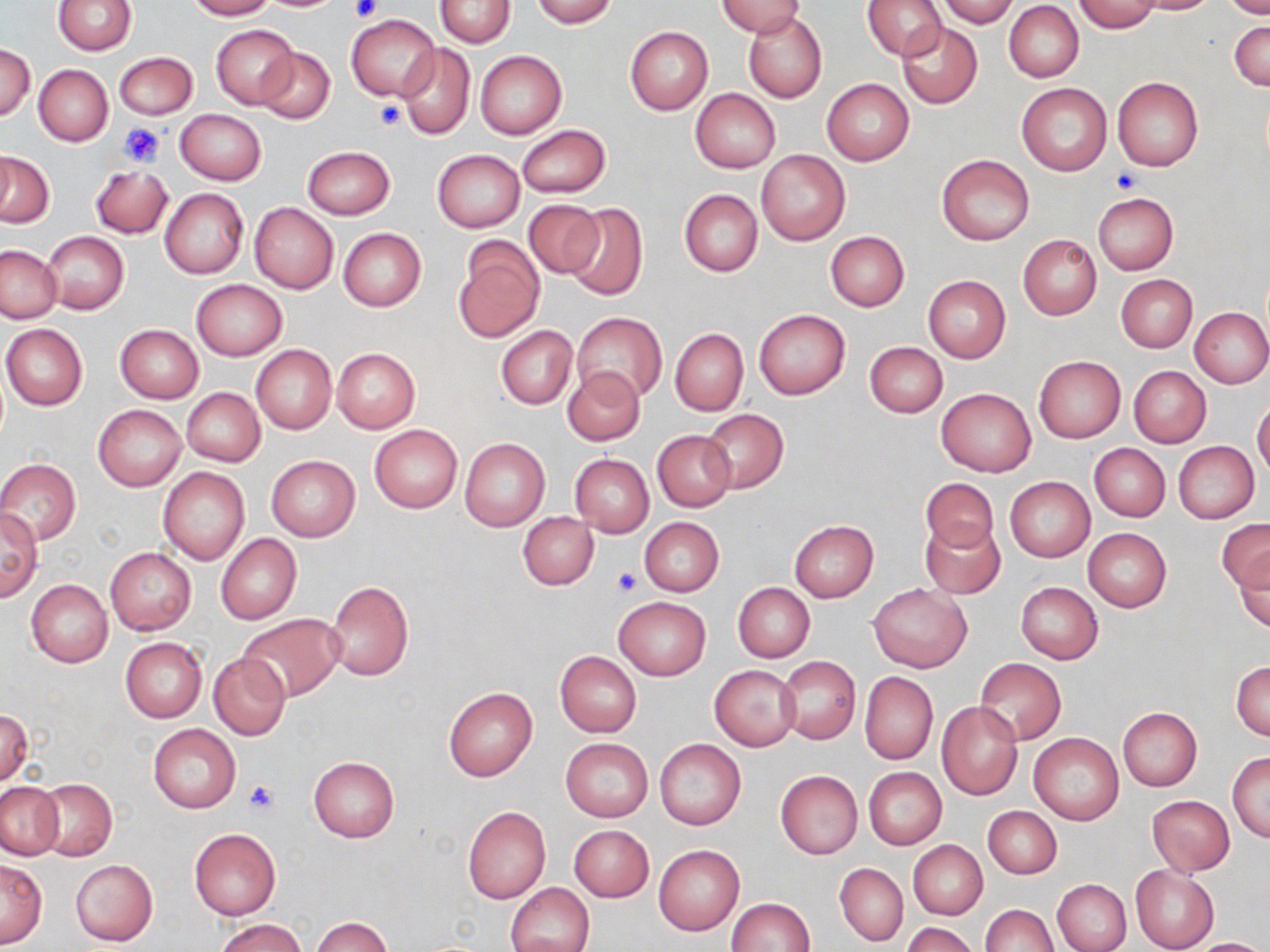
Approximate bounding boxes as [x1, y1, x2, y2] in pixels. Uninfected red blood cell locations: [53, 0, 135, 55], [184, 0, 275, 20], [435, 0, 515, 47], [531, 0, 619, 27], [715, 0, 807, 39], [863, 0, 948, 60], [937, 0, 1019, 27], [1128, 0, 1221, 14], [1219, 0, 1270, 19], [1071, 1, 1163, 33], [1004, 2, 1084, 82], [742, 11, 827, 104], [346, 14, 439, 102], [1229, 20, 1269, 90], [897, 22, 983, 108], [211, 24, 300, 109], [625, 25, 713, 115], [396, 42, 475, 139], [0, 44, 35, 121], [255, 47, 335, 123], [475, 51, 567, 138], [113, 52, 198, 120], [33, 64, 113, 145], [821, 78, 914, 165], [1112, 78, 1204, 171], [1017, 82, 1112, 175], [690, 88, 780, 174], [175, 109, 266, 185], [516, 124, 612, 198], [302, 146, 395, 219], [2, 147, 18, 222], [755, 148, 850, 245], [433, 150, 524, 233], [0, 151, 54, 227], [937, 153, 1033, 247], [90, 165, 172, 238], [159, 188, 248, 279], [679, 188, 763, 277], [1093, 192, 1178, 274], [523, 199, 604, 279], [248, 203, 339, 293], [563, 203, 648, 302], [338, 228, 426, 311], [825, 230, 910, 312], [42, 231, 128, 314], [1018, 235, 1101, 320], [454, 238, 545, 340], [1, 245, 62, 323], [1116, 274, 1197, 352], [923, 275, 1011, 362], [190, 279, 287, 360], [1189, 306, 1270, 388], [753, 308, 851, 400], [572, 312, 666, 405], [1, 323, 88, 410], [116, 324, 203, 403], [497, 326, 576, 409], [670, 328, 748, 415], [865, 341, 948, 417], [251, 345, 337, 434], [332, 348, 421, 434], [1034, 356, 1125, 442], [1129, 365, 1210, 447], [563, 367, 644, 444], [181, 388, 265, 468], [936, 388, 1035, 477], [1252, 398, 1270, 477], [93, 405, 186, 490], [699, 408, 789, 493], [369, 424, 463, 514], [651, 430, 737, 513], [459, 437, 550, 532], [1173, 441, 1259, 523], [1088, 442, 1170, 521], [569, 454, 653, 537], [266, 455, 359, 541], [0, 459, 81, 544], [157, 466, 250, 565], [919, 476, 998, 557], [1006, 476, 1096, 562], [0, 508, 43, 600], [517, 512, 599, 590], [639, 517, 724, 597], [790, 519, 879, 602], [920, 519, 1005, 599], [1217, 520, 1270, 593], [1083, 528, 1172, 611], [215, 533, 301, 625], [105, 547, 195, 635], [1232, 548, 1270, 631], [26, 580, 112, 667], [326, 580, 414, 681], [1015, 582, 1103, 664], [733, 583, 814, 663], [868, 583, 972, 673], [613, 597, 711, 679], [237, 613, 345, 702], [120, 637, 207, 723], [555, 651, 642, 737], [208, 652, 291, 740], [776, 657, 860, 743], [976, 658, 1066, 744], [1231, 660, 1270, 740], [710, 665, 802, 752], [860, 672, 937, 765], [443, 685, 537, 781], [936, 700, 1024, 800], [1117, 707, 1202, 791], [0, 709, 33, 789], [148, 723, 239, 813], [1029, 734, 1123, 824], [560, 738, 653, 822], [655, 739, 746, 830], [1228, 751, 1270, 843], [308, 755, 399, 842], [863, 767, 947, 850], [775, 770, 861, 858], [35, 779, 117, 862], [1, 782, 64, 860], [1147, 795, 1235, 876], [463, 806, 551, 904], [983, 806, 1061, 879], [568, 824, 654, 902], [189, 828, 281, 919], [908, 840, 987, 919], [654, 845, 744, 935], [0, 858, 47, 947], [71, 859, 158, 946], [835, 863, 907, 946], [1129, 865, 1219, 952], [1053, 879, 1131, 952], [505, 882, 595, 952], [727, 898, 814, 950], [982, 903, 1057, 951], [311, 916, 391, 952], [213, 917, 309, 952], [901, 922, 979, 952], [1186, 938, 1269, 952]. Platelet locations: [348, 0, 380, 22], [376, 100, 406, 128], [119, 123, 164, 167], [1112, 168, 1143, 194], [612, 568, 640, 596], [243, 780, 279, 815]. Slide-level diagnosis: negative for blood parasites. 1000x magnification. Thin blood film. Single field of view. Image is 1270×952 pixels. Light microscopy. May-Grünwald-Giemsa-stained preparation.